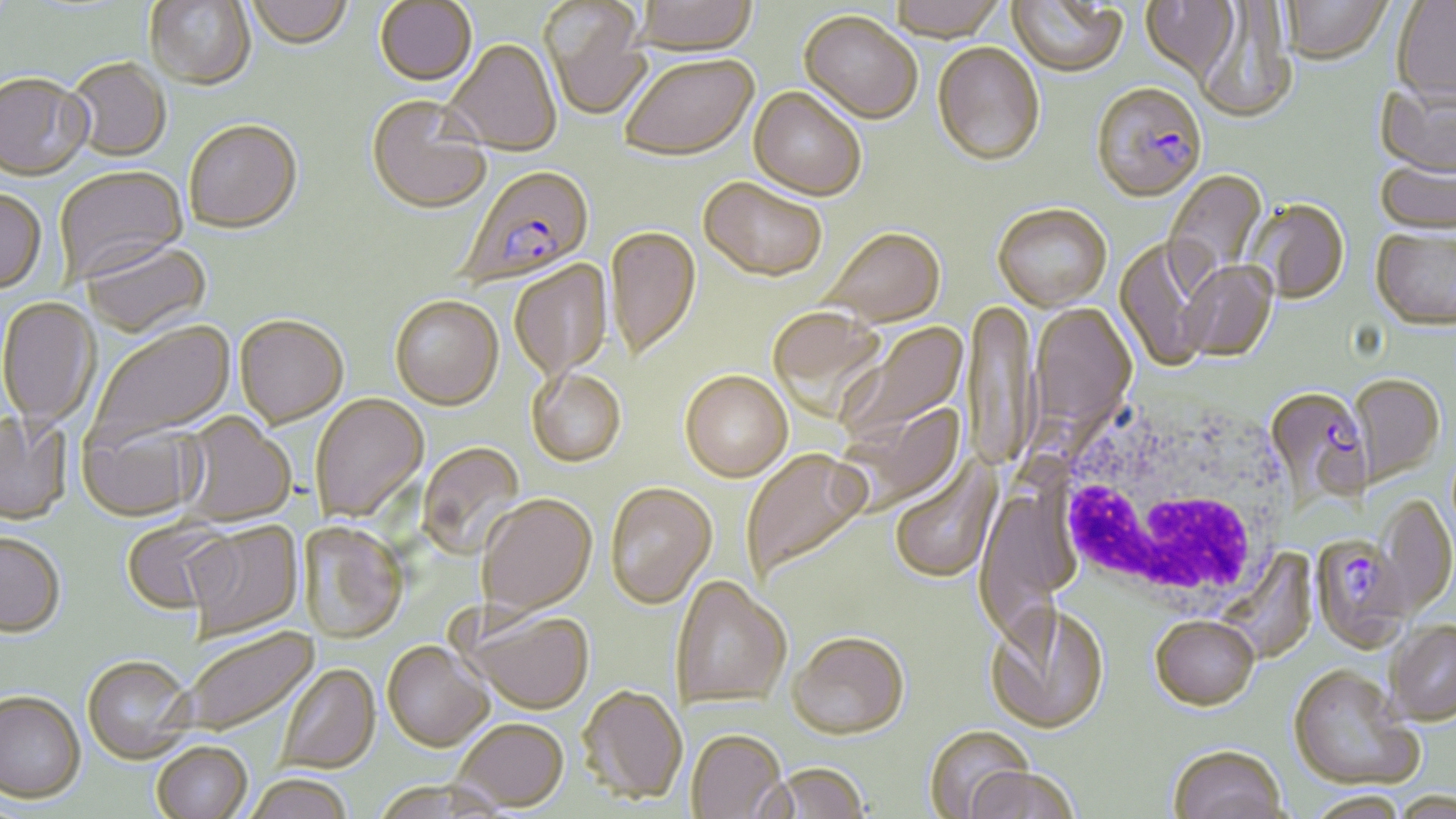
{
  "slide_level_diagnosis": "Plasmodium falciparum",
  "preparation": "thin blood smear",
  "image_size": "1456×819 pixels",
  "modality": "light microscopy",
  "plasmodium_falciparum_infected_red_blood_cell_locations": "approximate bounding boxes as (x1, y1, x2, y2) in pixels: (1090, 85, 1208, 205), (455, 167, 595, 291), (1265, 386, 1373, 511), (1310, 534, 1411, 654)",
  "magnification": "1000x",
  "white_blood_cell_locations": "approximate bounding boxes as (x1, y1, x2, y2) in pixels: (1045, 394, 1296, 618)",
  "field_of_view": "single",
  "stain": "May-Grünwald-Giemsa",
  "uninfected_red_blood_cell_locations": "approximate bounding boxes as (x1, y1, x2, y2) in pixels: (246, 0, 354, 52), (632, 0, 759, 57), (886, 0, 1008, 44), (1006, 0, 1130, 80), (1140, 0, 1241, 83), (1391, 0, 1456, 106), (144, 1, 256, 92), (539, 1, 653, 122), (1281, 1, 1393, 67), (374, 2, 477, 88), (1193, 3, 1298, 124), (799, 13, 922, 127), (444, 41, 562, 158), (932, 45, 1045, 168), (620, 57, 759, 164), (66, 60, 171, 164), (0, 76, 94, 184), (1375, 84, 1456, 180), (748, 89, 865, 201), (366, 98, 491, 217), (185, 122, 303, 237), (1375, 160, 1456, 239), (56, 167, 189, 284), (1164, 169, 1268, 292), (698, 178, 827, 283), (0, 191, 47, 295), (1248, 200, 1350, 305), (993, 204, 1112, 311), (604, 227, 701, 364), (819, 227, 946, 327), (1370, 230, 1456, 332), (1116, 237, 1218, 372), (82, 243, 211, 341), (510, 260, 614, 381), (1179, 262, 1278, 363), (389, 297, 503, 412), (0, 298, 98, 430), (966, 300, 1038, 475), (1030, 305, 1137, 434), (767, 307, 888, 420), (234, 317, 349, 431), (89, 322, 237, 449), (834, 322, 970, 447), (527, 370, 627, 468), (679, 371, 793, 483), (1348, 375, 1444, 489), (310, 394, 429, 524), (835, 402, 967, 516), (0, 412, 73, 527), (177, 413, 296, 526), (78, 420, 204, 523), (417, 442, 526, 560), (739, 448, 872, 582), (890, 454, 1003, 583), (604, 483, 717, 610), (1374, 493, 1456, 621), (477, 495, 598, 619), (122, 519, 234, 616), (185, 523, 303, 641), (300, 524, 409, 645), (0, 536, 64, 640), (1215, 549, 1316, 663), (671, 576, 791, 713), (984, 603, 1110, 735), (462, 609, 595, 716), (1150, 619, 1259, 714), (1386, 624, 1456, 728), (181, 628, 319, 737), (787, 635, 910, 743), (382, 643, 494, 755), (82, 659, 195, 766), (277, 665, 381, 775), (1287, 668, 1420, 793), (576, 687, 687, 807), (0, 695, 86, 806), (454, 720, 569, 813), (923, 727, 1035, 817), (686, 732, 787, 819), (152, 744, 252, 819), (1168, 746, 1289, 819), (763, 765, 871, 818), (964, 768, 1080, 819), (245, 778, 353, 819), (1307, 794, 1411, 819)"
}